Locate every Plasmodium parasite and every leukocyte.
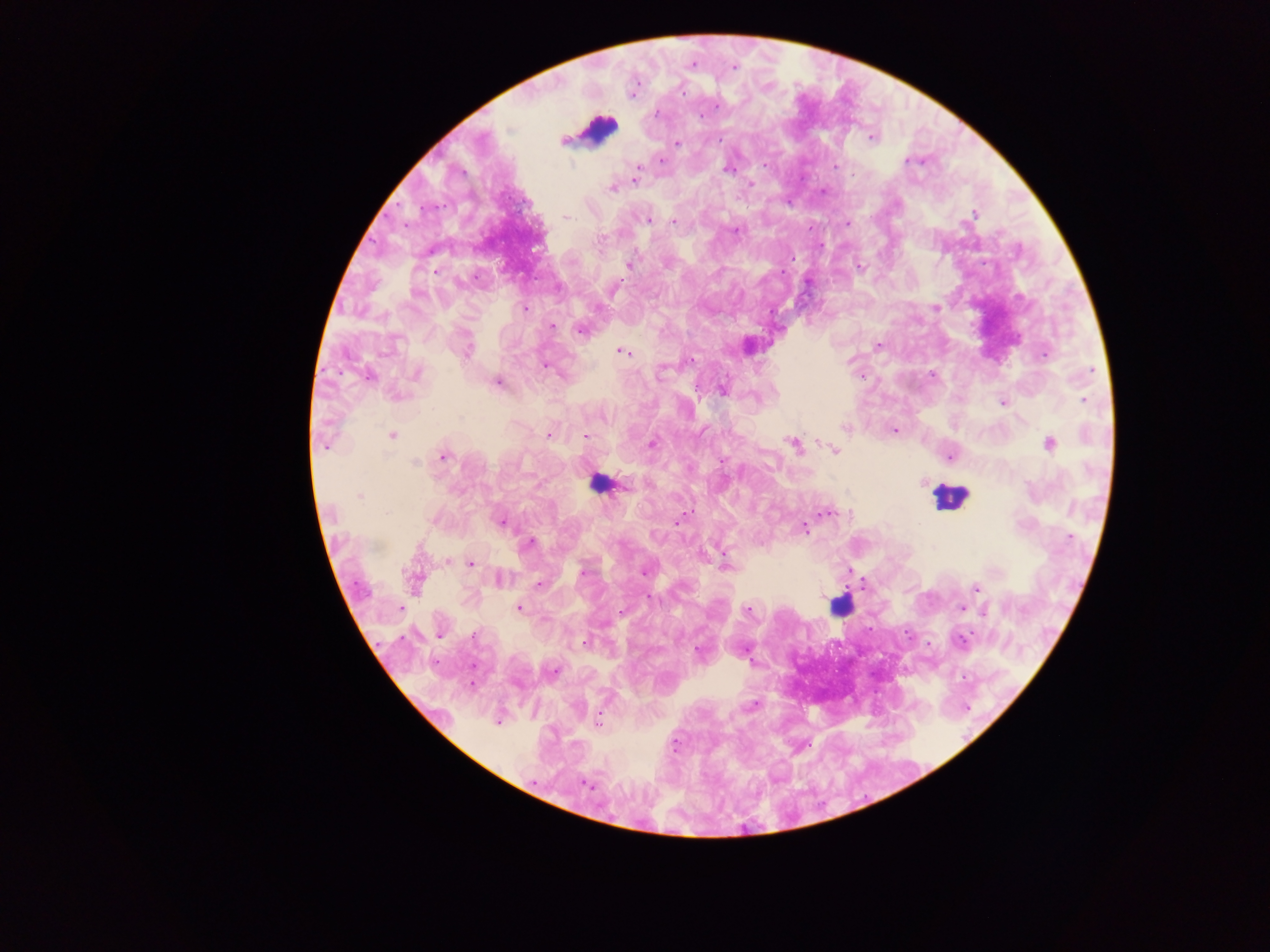
Approximate centers as x y in pixels.
Plasmodium parasites: 693 64; 733 67; 682 91; 717 105; 657 113; 871 136; 719 139; 563 142; 678 143; 661 160; 907 161; 834 167; 727 169; 638 170; 634 179; 751 185; 612 189; 822 192; 973 214; 566 217; 648 220; 674 221; 847 224; 735 231; 600 240; 793 257; 628 264; 861 268; 435 271; 615 289; 935 308; 525 309; 553 327; 580 331; 878 345; 467 351; 621 351; 1045 355; 692 360; 544 365; 661 371; 1090 371; 416 373; 932 375; 367 377; 498 383; 722 390; 1084 400; 1003 403; 845 427; 894 430; 548 435; 392 436; 585 436; 652 444; 793 444; 1050 444; 325 445; 834 450; 443 457; 950 457; 722 461; 415 463; 924 482; 626 484; 359 497; 828 513; 678 521; 501 522; 804 528; 1070 538; 529 543; 448 562; 471 564; 725 564; 583 571; 644 572; 538 585; 976 588; 649 597; 400 609; 519 609; 962 609; 747 610; 982 611; 440 635; 474 635; 961 640; 585 643; 699 651; 554 672; 753 705; 498 722; 597 722; 587 784.
Leukocytes: 598 128; 598 486; 951 497; 838 606.

image size = 1270×952 pixels
preparation = thick blood smear
capture = mobile-phone photograph through a microscope
country = Ghana
field of view = single